Assess the morphology of the red blood cells.
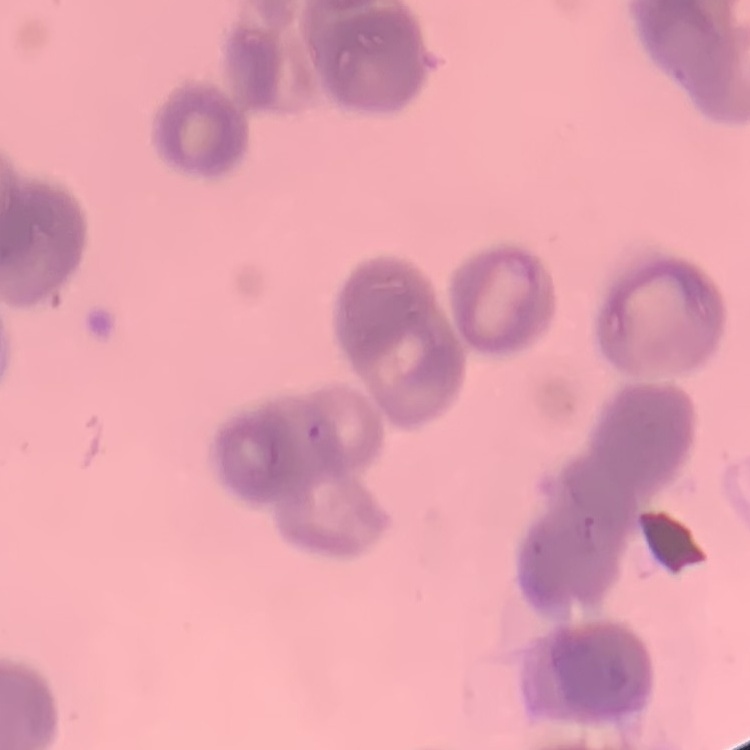

Rouleaux formation.

Summary:
  - Stain: Field's or Giemsa
  - Preparation: thin blood smear
  - Image type: one tile cut from a larger photomicrograph